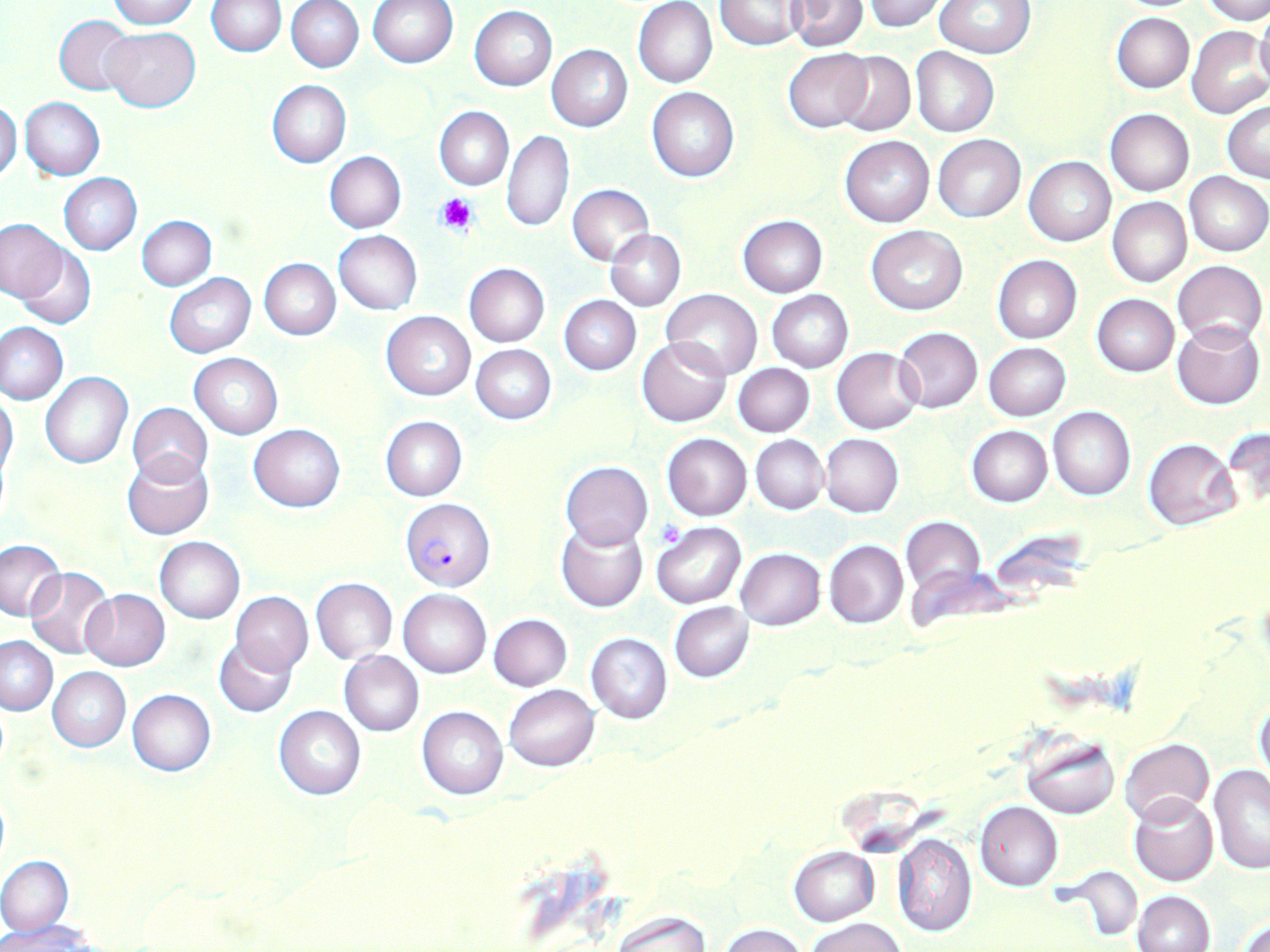
slide-level diagnosis = Plasmodium falciparum
stain = May-Grünwald-Giemsa
magnification = 1000x
preparation = thin blood smear
uninfected red blood cell locations (subset) = approximate bounding boxes as named x1/y1/x2/y2 corners in pixels: (x1=107, y1=0, x2=198, y2=28), (x1=367, y1=0, x2=457, y2=69), (x1=714, y1=0, x2=807, y2=50), (x1=786, y1=0, x2=867, y2=50), (x1=862, y1=0, x2=945, y2=32), (x1=1202, y1=0, x2=1270, y2=25), (x1=207, y1=1, x2=287, y2=56), (x1=287, y1=1, x2=364, y2=73), (x1=632, y1=1, x2=718, y2=88), (x1=934, y1=1, x2=1034, y2=58), (x1=469, y1=6, x2=557, y2=90), (x1=1253, y1=7, x2=1270, y2=90), (x1=1112, y1=12, x2=1195, y2=92), (x1=54, y1=15, x2=137, y2=96), (x1=102, y1=26, x2=201, y2=112), (x1=1186, y1=26, x2=1269, y2=119), (x1=546, y1=44, x2=633, y2=132), (x1=911, y1=47, x2=999, y2=136), (x1=782, y1=48, x2=874, y2=134), (x1=833, y1=50, x2=915, y2=136), (x1=266, y1=79, x2=351, y2=168), (x1=647, y1=87, x2=739, y2=182), (x1=20, y1=98, x2=105, y2=180), (x1=0, y1=100, x2=22, y2=182), (x1=1222, y1=101, x2=1270, y2=182), (x1=433, y1=107, x2=513, y2=190), (x1=1105, y1=109, x2=1194, y2=195), (x1=502, y1=128, x2=573, y2=232), (x1=933, y1=135, x2=1025, y2=222), (x1=840, y1=136, x2=934, y2=226), (x1=325, y1=151, x2=406, y2=232), (x1=1024, y1=155, x2=1116, y2=246), (x1=1185, y1=170, x2=1269, y2=256), (x1=59, y1=173, x2=142, y2=255), (x1=567, y1=183, x2=654, y2=266), (x1=1108, y1=197, x2=1191, y2=287), (x1=138, y1=215, x2=217, y2=290), (x1=738, y1=215, x2=828, y2=295), (x1=0, y1=217, x2=66, y2=303), (x1=866, y1=225, x2=967, y2=314), (x1=605, y1=229, x2=686, y2=312), (x1=334, y1=230, x2=422, y2=315), (x1=16, y1=245, x2=97, y2=329), (x1=991, y1=255, x2=1081, y2=343), (x1=259, y1=258, x2=340, y2=340), (x1=1173, y1=259, x2=1267, y2=345), (x1=464, y1=264, x2=550, y2=347), (x1=165, y1=274, x2=256, y2=357), (x1=663, y1=288, x2=763, y2=379), (x1=767, y1=290, x2=854, y2=372), (x1=559, y1=295, x2=640, y2=375), (x1=1091, y1=295, x2=1179, y2=377), (x1=381, y1=310, x2=475, y2=401), (x1=1172, y1=321, x2=1265, y2=409), (x1=1, y1=322, x2=68, y2=404), (x1=894, y1=327, x2=982, y2=413), (x1=636, y1=336, x2=732, y2=427), (x1=984, y1=342, x2=1071, y2=421), (x1=470, y1=345, x2=555, y2=424), (x1=295, y1=346, x2=381, y2=438), (x1=832, y1=347, x2=923, y2=435), (x1=189, y1=353, x2=283, y2=439), (x1=733, y1=363, x2=815, y2=437), (x1=40, y1=371, x2=133, y2=469), (x1=0, y1=392, x2=19, y2=482), (x1=127, y1=402, x2=213, y2=485), (x1=1048, y1=407, x2=1134, y2=500), (x1=381, y1=416, x2=467, y2=501), (x1=248, y1=424, x2=345, y2=512), (x1=1223, y1=424, x2=1270, y2=517), (x1=967, y1=426, x2=1052, y2=506), (x1=662, y1=433, x2=752, y2=521), (x1=751, y1=434, x2=828, y2=514), (x1=821, y1=434, x2=903, y2=517), (x1=1144, y1=438, x2=1240, y2=531), (x1=122, y1=450, x2=214, y2=540), (x1=561, y1=462, x2=652, y2=549), (x1=900, y1=517, x2=985, y2=597), (x1=555, y1=520, x2=648, y2=613), (x1=650, y1=522, x2=745, y2=609), (x1=154, y1=536, x2=245, y2=622), (x1=0, y1=537, x2=70, y2=622), (x1=824, y1=539, x2=909, y2=629), (x1=736, y1=548, x2=825, y2=630), (x1=25, y1=566, x2=115, y2=660), (x1=311, y1=577, x2=397, y2=663), (x1=80, y1=588, x2=170, y2=672), (x1=398, y1=588, x2=491, y2=677), (x1=231, y1=592, x2=313, y2=674), (x1=669, y1=602, x2=753, y2=682), (x1=488, y1=613, x2=572, y2=691), (x1=586, y1=633, x2=672, y2=724), (x1=1, y1=635, x2=58, y2=716), (x1=214, y1=635, x2=299, y2=718), (x1=339, y1=650, x2=425, y2=737), (x1=48, y1=667, x2=131, y2=751), (x1=504, y1=685, x2=598, y2=771), (x1=127, y1=689, x2=216, y2=776), (x1=1253, y1=698, x2=1270, y2=788), (x1=275, y1=706, x2=365, y2=799), (x1=418, y1=706, x2=508, y2=799), (x1=1022, y1=734, x2=1120, y2=819), (x1=1121, y1=737, x2=1213, y2=822), (x1=1208, y1=767, x2=1270, y2=875), (x1=1130, y1=794, x2=1219, y2=886), (x1=976, y1=801, x2=1063, y2=890), (x1=892, y1=832, x2=978, y2=939), (x1=789, y1=846, x2=879, y2=925), (x1=0, y1=855, x2=73, y2=936), (x1=1059, y1=866, x2=1145, y2=943), (x1=1132, y1=891, x2=1214, y2=952), (x1=610, y1=911, x2=709, y2=951), (x1=1235, y1=915, x2=1270, y2=952), (x1=807, y1=918, x2=907, y2=952), (x1=4, y1=921, x2=96, y2=951), (x1=719, y1=923, x2=806, y2=951)
platelet locations = approximate bounding boxes as named x1/y1/x2/y2 corners in pixels: (x1=435, y1=193, x2=478, y2=235), (x1=657, y1=520, x2=685, y2=547)
modality = light microscopy
image size = 1270×952 pixels
field of view = one of a larger specimen